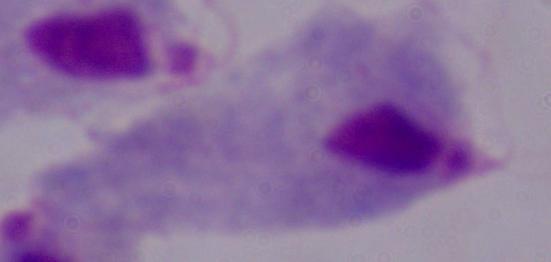

{
  "identification": "trichomonad",
  "modality": "micrograph",
  "magnification": "1000x"
}